Identify the cell.
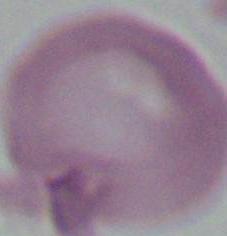
This is an erythrocyte.

Micrograph. 1000x magnification.